Name the parasite shown.
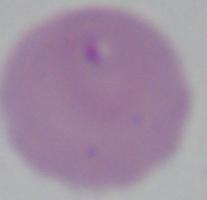

This is Babesia.

Captured at 1000x magnification. Micrograph.